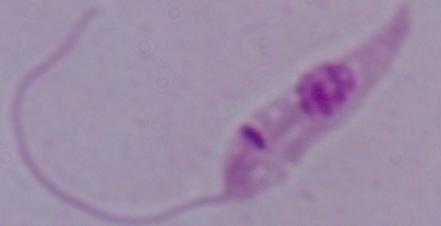

Summary:
  - Identification: Leishmania
  - Modality: photomicrograph
  - Magnification: 1000x